Locate every blood parasite and identify its species.
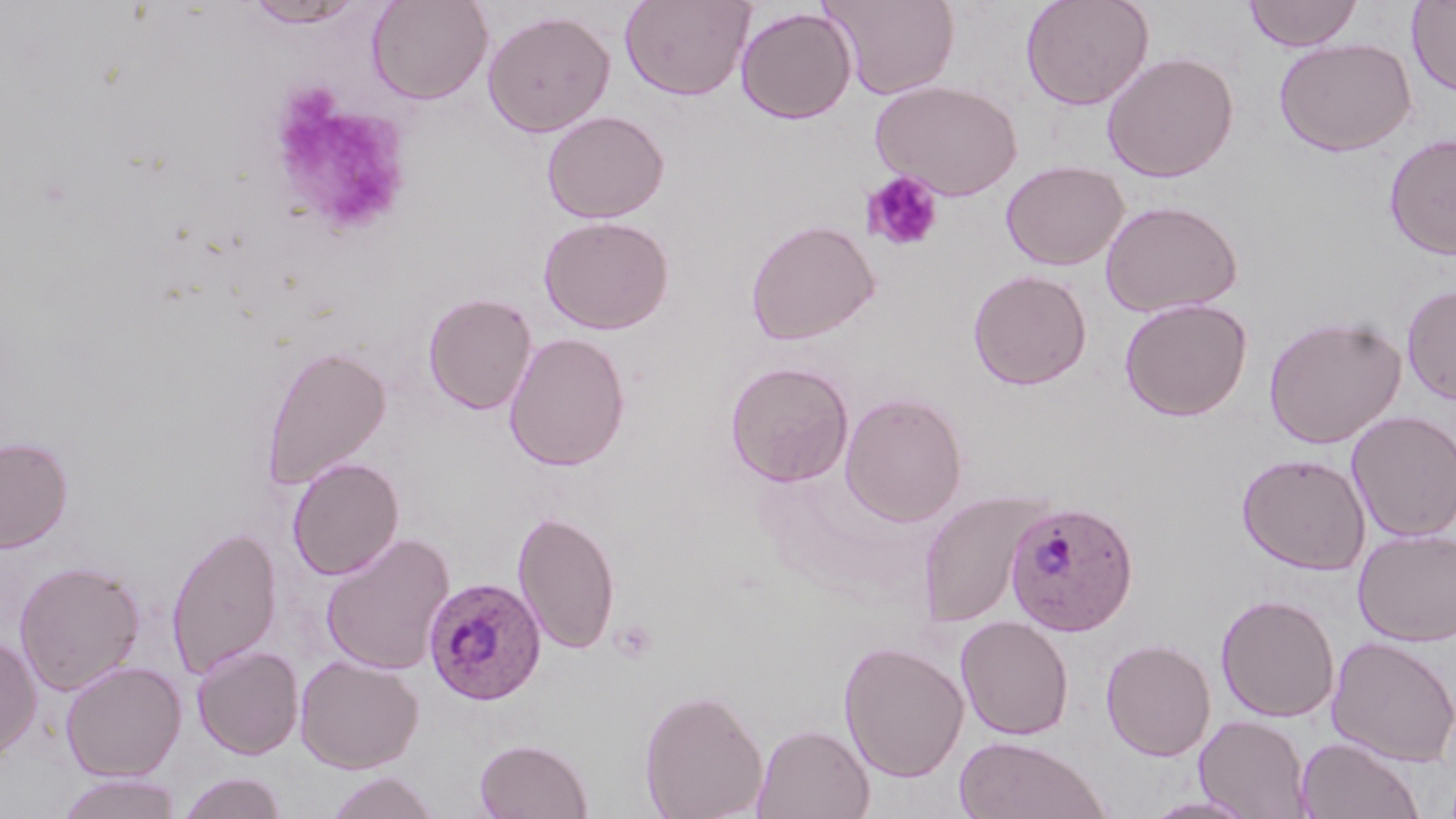
Approximate bounding boxes as (x1, y1, x2, y2) in pixels.
Plasmodium ovale-infected red blood cells: (1004, 500, 1139, 636), (423, 577, 547, 704).
No Plasmodium falciparum, Plasmodium malariae, Plasmodium vivax, Babesia divergens, or Trypanosoma brucei observed.

Uninfected red blood cell locations: (367, 0, 492, 104), (619, 0, 755, 101), (825, 0, 960, 99), (1020, 0, 1155, 111), (1241, 0, 1364, 51), (1406, 0, 1456, 97), (240, 1, 369, 29), (735, 6, 857, 124), (482, 10, 616, 137), (1273, 37, 1418, 157), (1102, 51, 1239, 182), (870, 80, 1023, 200), (541, 110, 669, 223), (1384, 133, 1456, 260), (1000, 160, 1128, 271), (1100, 199, 1243, 317), (538, 215, 675, 335), (745, 219, 880, 345), (967, 270, 1092, 390), (1401, 284, 1456, 406), (423, 292, 537, 415), (1119, 297, 1253, 420), (1263, 315, 1407, 449), (503, 332, 631, 471), (260, 344, 391, 490), (725, 361, 854, 487), (840, 392, 967, 526), (1347, 410, 1456, 542), (0, 435, 73, 553), (1237, 452, 1370, 575), (287, 456, 404, 581), (919, 490, 1040, 628), (512, 508, 620, 656), (166, 524, 283, 680), (1354, 528, 1456, 646), (320, 532, 455, 676), (14, 560, 145, 696), (1215, 594, 1340, 723), (955, 615, 1075, 740), (0, 634, 42, 763), (1326, 635, 1456, 767), (1101, 639, 1216, 761), (838, 640, 969, 783), (191, 644, 303, 760), (294, 654, 424, 773), (60, 661, 186, 781), (639, 686, 768, 819), (1194, 714, 1311, 818), (751, 723, 874, 819), (953, 735, 1110, 819), (1294, 735, 1426, 819), (474, 738, 593, 818), (324, 771, 442, 818), (176, 772, 288, 819), (55, 773, 183, 818), (1138, 794, 1260, 818). Platelet locations: (264, 86, 414, 238), (861, 171, 943, 252), (610, 621, 657, 664). Slide-level diagnosis: Plasmodium ovale. Single field of view. Thin blood smear. Optical microscopy. May-Grünwald-Giemsa stain. 1000x magnification. Image is 1456×819 pixels.